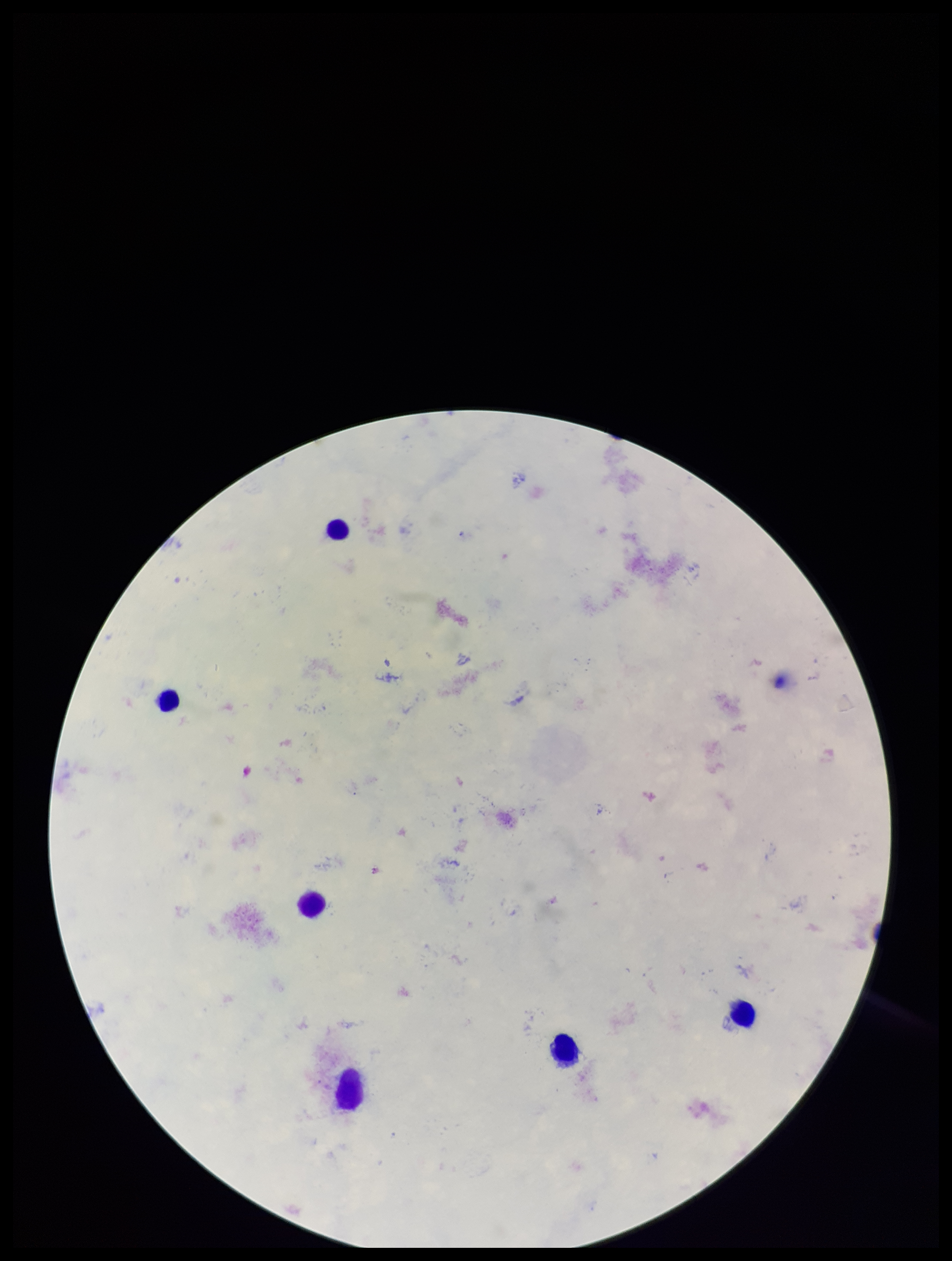

Summary:
  - Plasmodium parasites: none seen
  - Preparation: thick
  - Stain: Giemsa
  - Image size: 952×1261 pixels
  - Field of view: single
  - Patient malaria status: negative
  - Parasite count: 0
  - Leukocyte count: 6
  - Capture: smartphone photograph through the microscope eyepiece